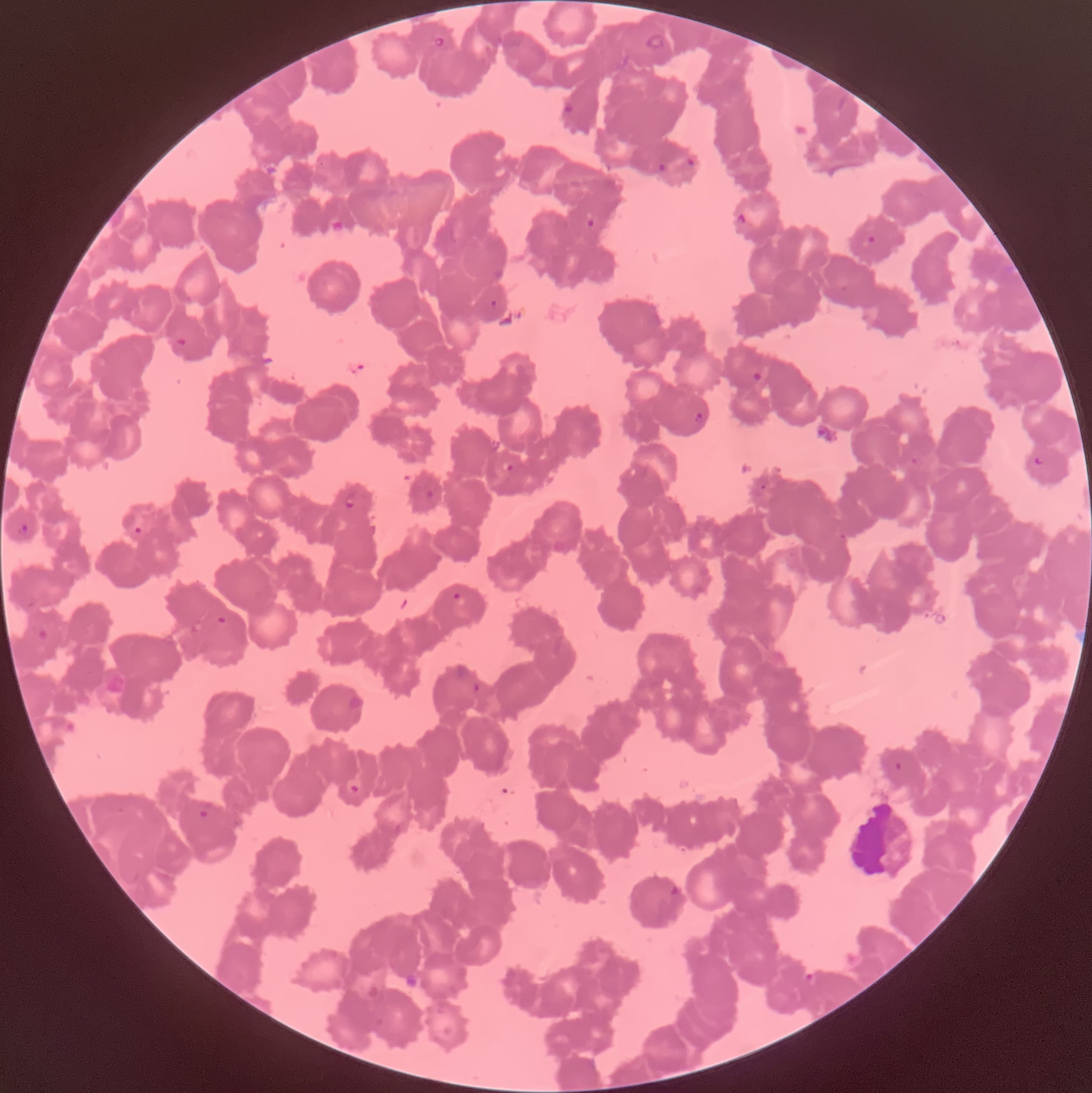
Summary:
  - Coordinate format: approximate bounding boxes as (x1, y1, x2, y2) in pixels
  - Plasmodium parasite locations: (431, 35, 448, 48), (563, 100, 576, 114), (683, 160, 698, 181), (657, 162, 668, 172), (738, 211, 755, 226), (586, 219, 596, 227), (861, 236, 876, 250), (490, 299, 497, 309), (177, 337, 187, 346), (752, 369, 764, 382), (695, 411, 704, 423), (1034, 455, 1045, 466), (911, 457, 925, 466), (501, 459, 516, 474), (425, 489, 434, 499), (345, 491, 357, 509), (16, 523, 30, 536), (134, 525, 142, 535), (450, 591, 462, 603), (215, 614, 229, 627), (470, 681, 483, 695), (349, 784, 360, 794), (198, 805, 210, 818), (671, 884, 681, 899), (801, 971, 816, 983)
  - Plasmodium parasites too small for a box (approximate centers as (x, y) in pixels): (764, 486)
  - Image size: 1092×1093 pixels
  - Preparation: thin blood smear
  - Modality: optical microscopy
  - Red blood cell morphology: rouleaux formation